State which parasite is depicted.
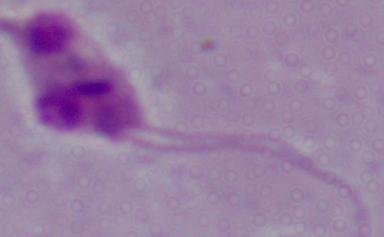
Leishmania.

Photomicrograph. 1000x magnification.